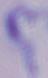 A trypanosome is shown. Micrograph. 1000x magnification.